Report the malaria status of this cell.
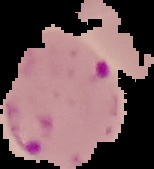

It is parasitized.

Summary:
  - Preparation: thin blood smear
  - Image type: cell region segmented out of the field of view; surrounding area masked to black
  - Image size: 154×169 pixels